Locate every Trypanosoma brucei.
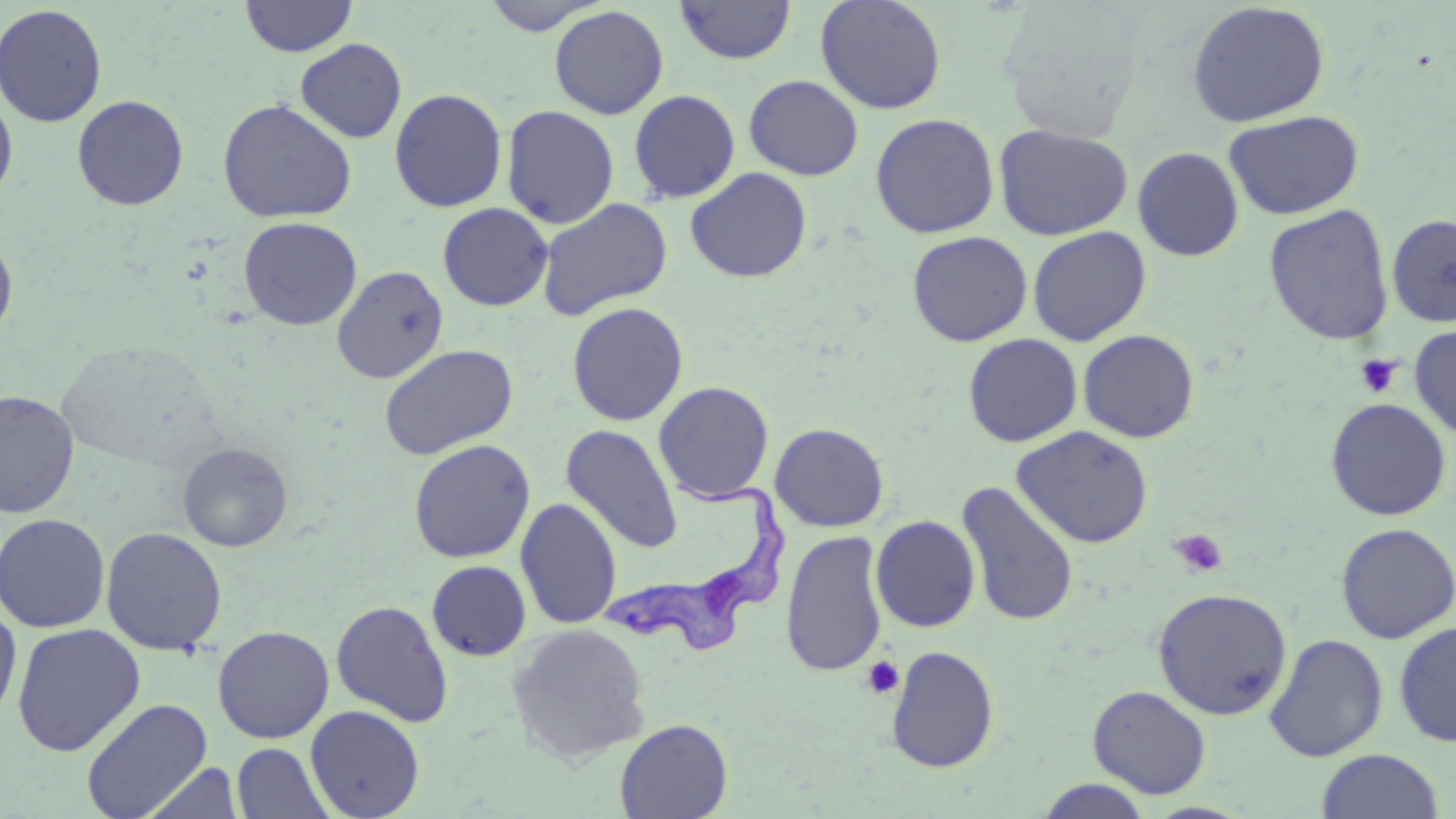

Approximate bounding boxes as (x1, y1, x2, y2) in pixels.
Trypanosoma brucei: (599, 472, 800, 656).

slide-level diagnosis = Trypanosoma brucei
image size = 1456×819 pixels
stain = May-Grünwald-Giemsa
platelet locations = approximate bounding boxes as (x1, y1, x2, y2) in pixels: (1355, 354, 1401, 399), (1170, 529, 1229, 578), (861, 656, 905, 699)
magnification = 1000x
field of view = one of a larger specimen
uninfected red blood cell locations = approximate bounding boxes as (x1, y1, x2, y2) in pixels: (240, 0, 358, 57), (480, 0, 609, 35), (675, 0, 796, 64), (814, 0, 947, 114), (1186, 1, 1331, 128), (0, 4, 108, 127), (996, 4, 1148, 140), (549, 5, 669, 120), (294, 38, 407, 143), (744, 74, 864, 180), (389, 88, 508, 212), (0, 89, 18, 206), (629, 89, 741, 204), (71, 94, 189, 211), (217, 98, 357, 224), (501, 104, 619, 229), (1223, 110, 1364, 220), (870, 112, 1000, 238), (993, 124, 1133, 240), (1132, 146, 1244, 262), (685, 167, 812, 283), (536, 197, 673, 321), (437, 202, 554, 311), (1263, 204, 1395, 346), (1386, 214, 1456, 327), (238, 216, 362, 331), (1028, 226, 1152, 345), (907, 231, 1033, 346), (0, 232, 18, 343), (331, 265, 448, 384), (567, 302, 688, 426), (1409, 324, 1456, 440), (1077, 329, 1200, 443), (963, 333, 1082, 447), (379, 344, 517, 460), (653, 381, 775, 503), (0, 389, 79, 518), (1325, 397, 1452, 521), (770, 422, 889, 532), (561, 425, 684, 554), (1012, 425, 1154, 548), (409, 439, 535, 562), (178, 442, 293, 552), (956, 480, 1079, 627), (516, 497, 622, 630), (0, 513, 111, 633), (871, 515, 981, 633), (1335, 522, 1455, 644), (100, 526, 228, 655), (780, 530, 888, 678), (426, 560, 532, 661), (1152, 587, 1292, 720), (331, 600, 454, 727), (0, 601, 22, 726), (1393, 621, 1456, 747), (12, 623, 145, 756), (507, 623, 651, 765), (212, 626, 334, 744), (1264, 633, 1388, 761), (885, 645, 999, 773), (1087, 685, 1211, 798), (80, 697, 212, 818), (305, 705, 425, 819), (614, 718, 734, 819), (232, 742, 334, 819), (1316, 749, 1444, 818), (138, 761, 245, 819), (1035, 779, 1153, 818)
modality = light microscopy
preparation = thin blood film